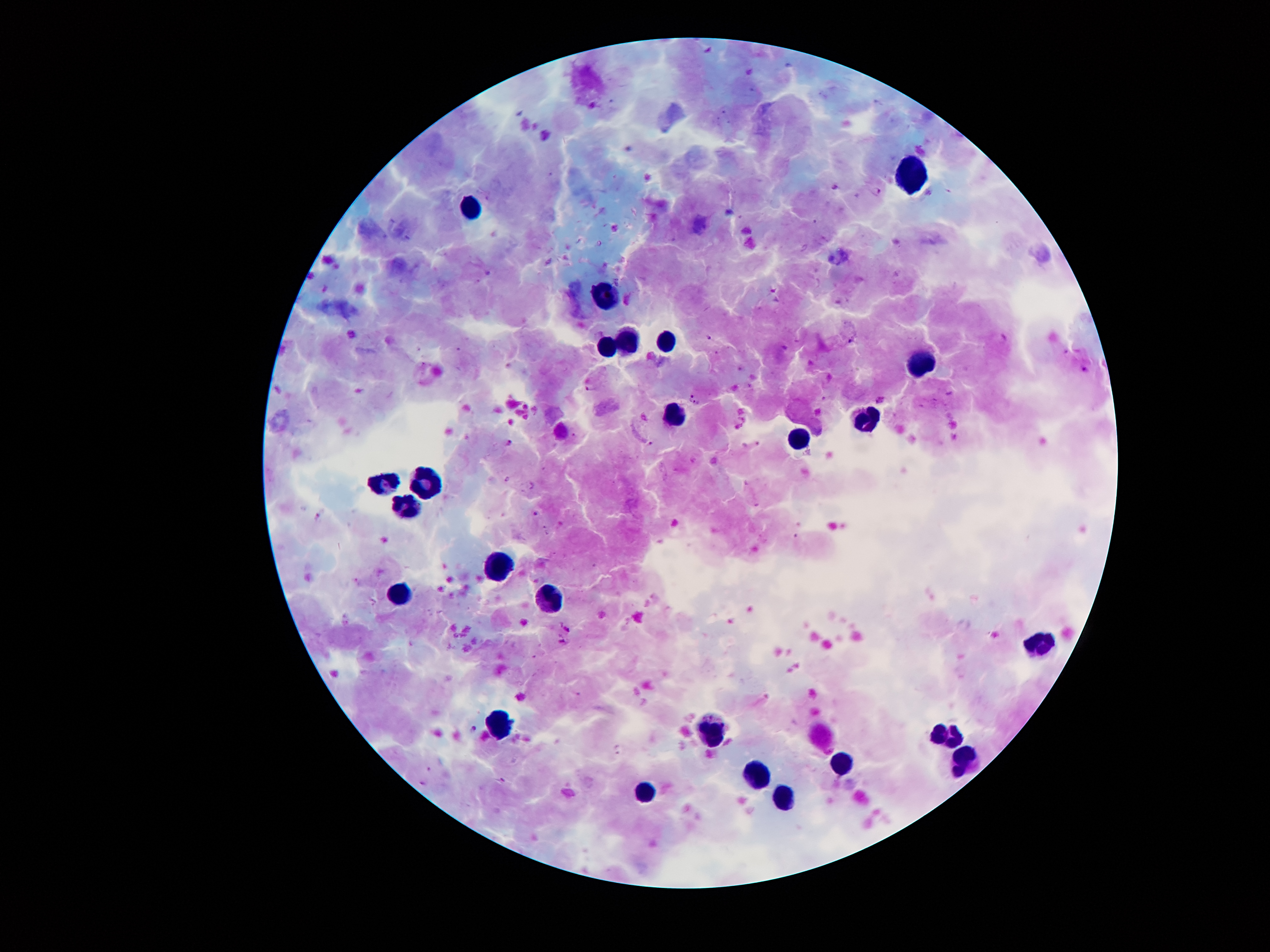
coordinate format = approximate object centers, in pixels from the top-left corner
leukocyte locations = (x=911, y=176), (x=475, y=208), (x=606, y=299), (x=664, y=343), (x=630, y=344), (x=608, y=349), (x=924, y=361), (x=675, y=415), (x=870, y=418), (x=798, y=439), (x=424, y=480), (x=389, y=484), (x=412, y=499), (x=499, y=568), (x=398, y=594), (x=553, y=601), (x=1046, y=647), (x=711, y=729), (x=951, y=732), (x=966, y=759), (x=838, y=766), (x=763, y=780), (x=647, y=791), (x=787, y=795)
Plasmodium parasite locations = (x=544, y=135), (x=836, y=186), (x=876, y=191), (x=488, y=273), (x=710, y=337), (x=1004, y=339), (x=850, y=341), (x=589, y=389), (x=690, y=396), (x=880, y=399), (x=696, y=403), (x=509, y=442), (x=651, y=444), (x=508, y=479), (x=536, y=513), (x=568, y=629), (x=561, y=642), (x=475, y=729), (x=501, y=781)
patient malaria status = infected with Plasmodium falciparum
magnification = 100x
image size = 1270×952 pixels
capture = smartphone through the microscope eyepiece
preparation = thick blood film
stain = Giemsa
field of view = one from this slide